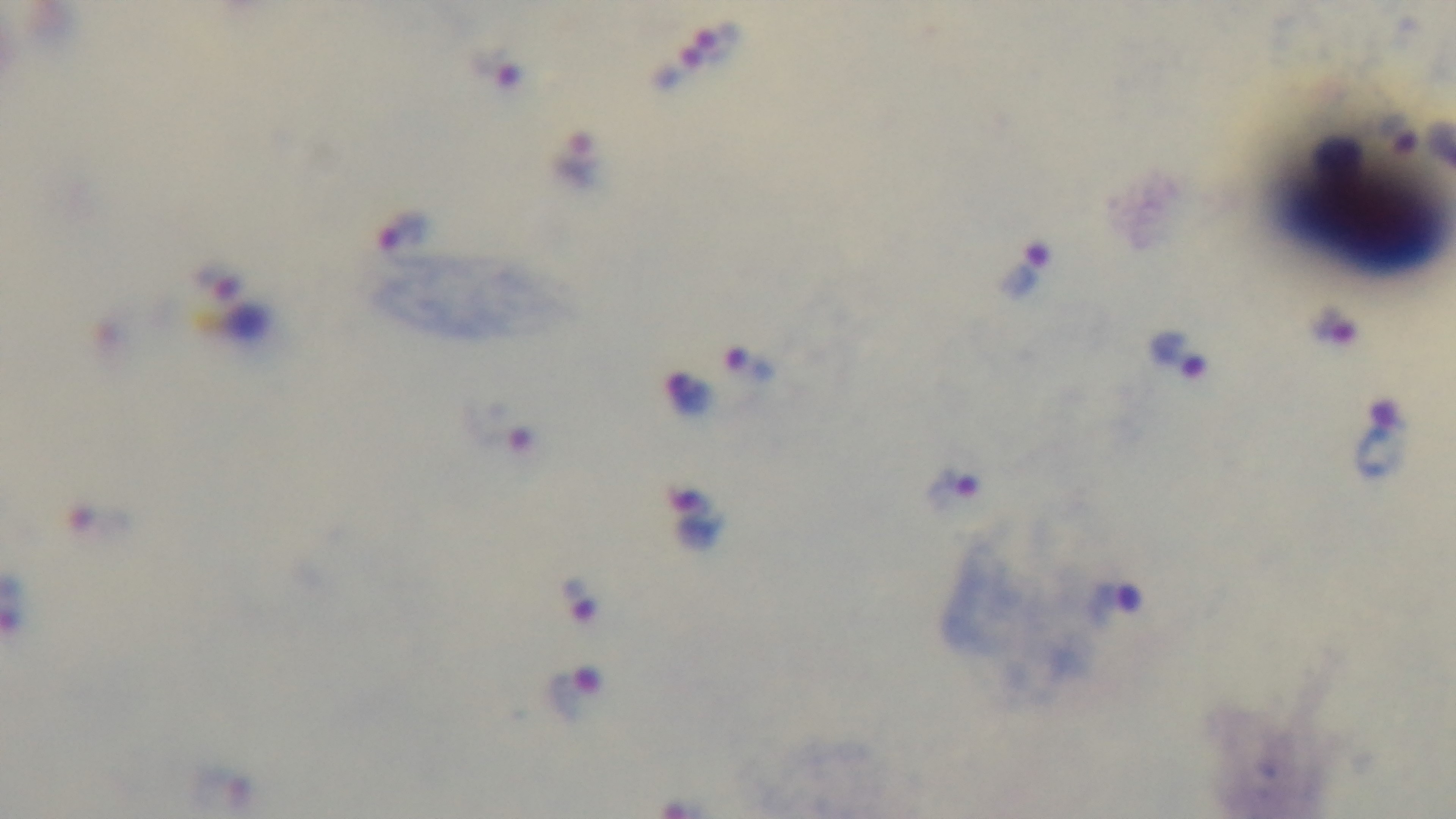

malaria status = positive
objective = 100x oil immersion
stain = Giemsa
field of view = single
capture = mounted 4K digital camera
modality = light microscopy
preparation = thick blood film